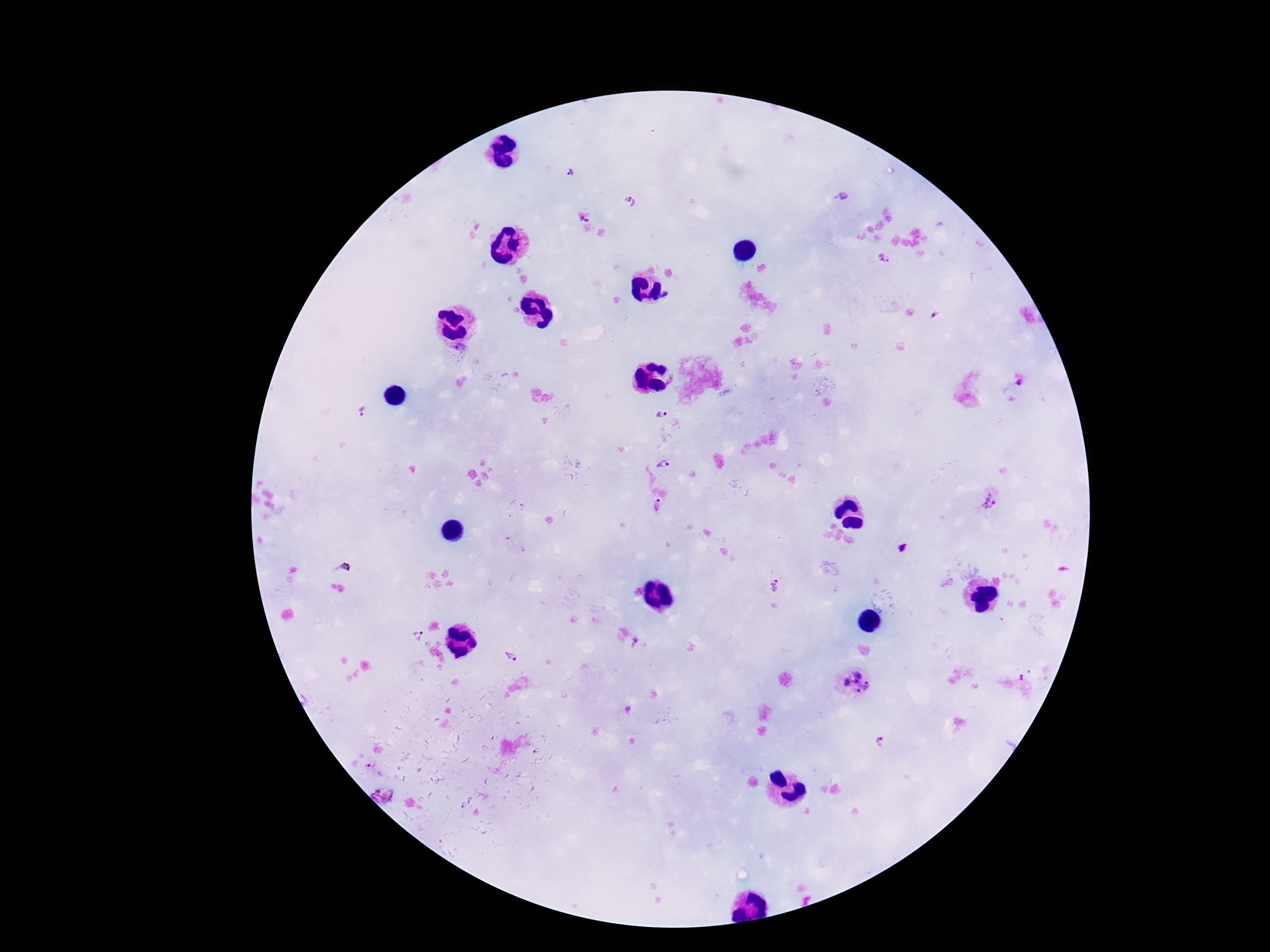

Approximate centers as {x, y} in pixels. Plasmodium parasite locations: {571, 173}, {844, 197}, {632, 201}, {585, 218}, {884, 259}, {462, 349}, {1020, 384}, {362, 412}, {661, 416}, {665, 465}, {991, 500}, {659, 506}, {903, 549}, {342, 569}, {775, 586}, {417, 635}, {635, 642}, {511, 658}, {855, 682}, {881, 743}. 100x magnification. One field from this slide. Giemsa stain. Thick blood film. Patient malaria status: infected. Image is 1270×952 pixels. Photographed through the microscope eyepiece with a smartphone camera.